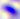 Toxoplasma gondii is seen. Captured at 400x magnification. Micrograph.